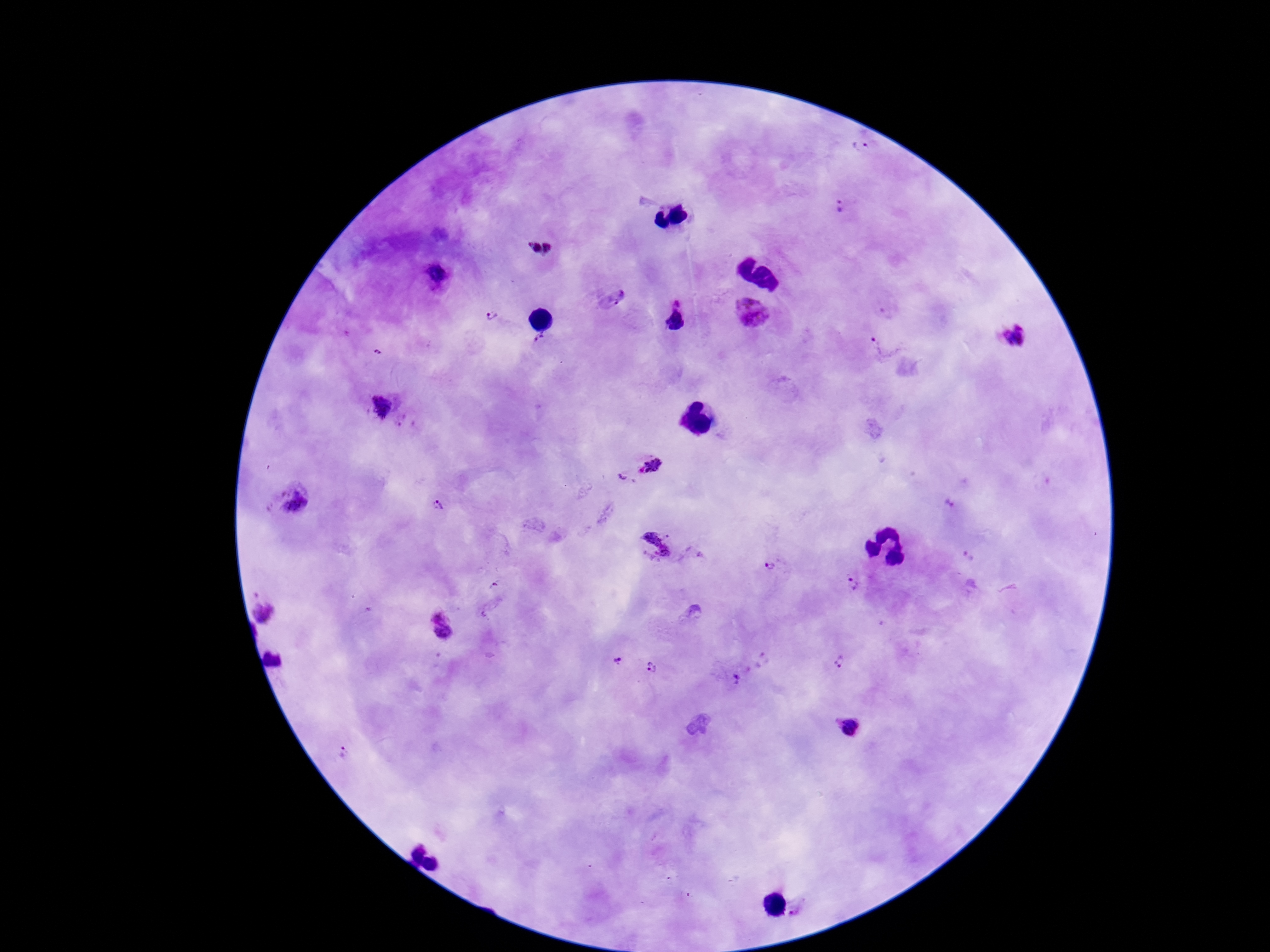

{
  "stain": "Giemsa",
  "magnification": "100x",
  "capture": "smartphone camera through the microscope eyepiece",
  "patient_malaria_status": "positive",
  "image_size": "1270×952 pixels",
  "plasmodium_parasite_locations": "approximate centers as [x, y] in pixels: [862, 144], [843, 207], [534, 248], [548, 248], [437, 275], [616, 297], [678, 301], [751, 311], [493, 317], [1014, 335], [541, 340], [883, 343], [384, 406], [407, 421], [654, 464], [626, 480], [291, 501], [950, 505], [436, 508], [653, 545], [770, 567], [853, 584], [265, 611], [692, 611], [442, 628], [272, 661], [619, 662], [839, 662], [652, 668], [736, 681], [850, 725], [343, 751]",
  "preparation": "thick blood smear",
  "field_of_view": "one from this slide"
}